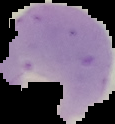

Cell region segmented out of the field of view; the surrounding area is masked to black. From a thin blood smear. Image is 115×124 pixels. Malaria status: parasitized.